Describe the morphology of the erythrocytes.
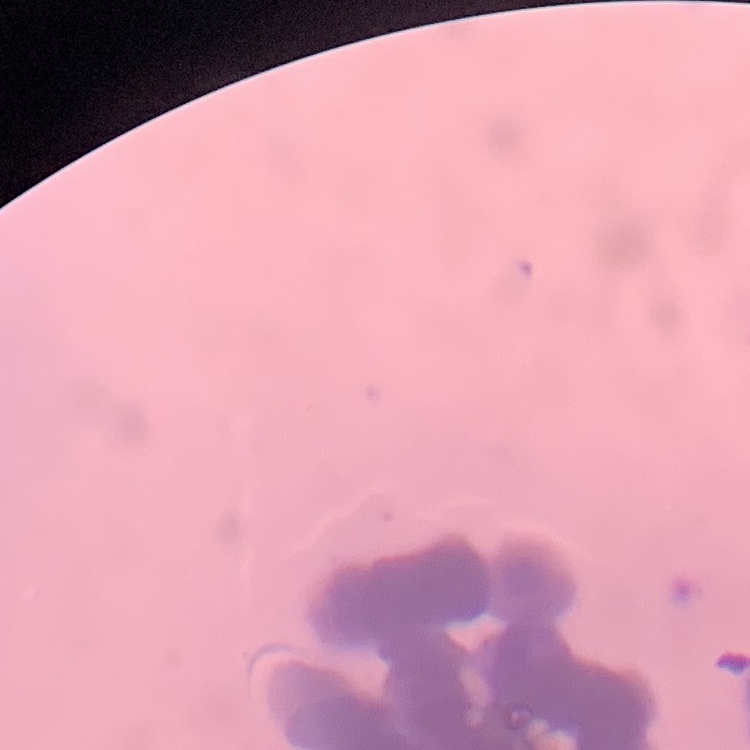
They show rouleaux formation.

preparation = thin blood film
image type = one tile cut from a larger photomicrograph
stain = Field's or Giemsa